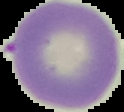
Summary:
  - Preparation: thin blood film
  - Image type: segmented cell region on a black background
  - Result: negative for Plasmodium parasites
  - Image size: 124×112 pixels